Classify this cell by malaria status.
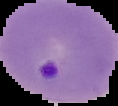

Parasitized.

Summary:
  - Image type: cell region segmented out of the field of view; surrounding area masked to black
  - Image size: 118×106 pixels
  - Preparation: thin blood film